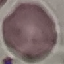
Summary:
  - Malaria status: uninfected
  - Image type: cell patch, automatically extracted from a larger field of view and resized to 64 × 64 pixels
  - Preparation: thin smear
  - Capture: smartphone camera at the microscope eyepiece
  - Stain: Giemsa